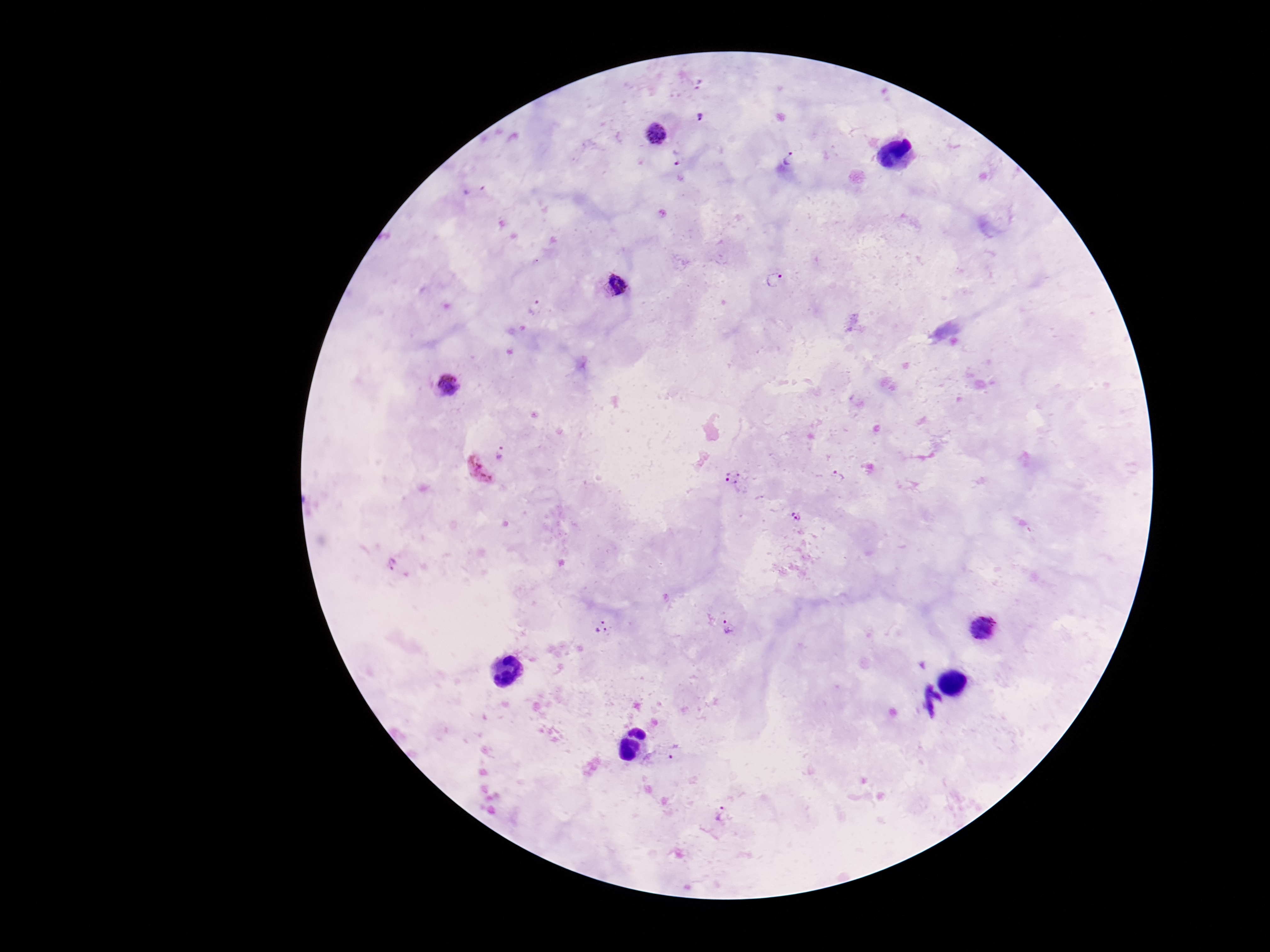

Approximate object centers, in pixels from the top-left corner. Plasmodium parasite locations: (x=697, y=83), (x=699, y=116), (x=656, y=133), (x=679, y=158), (x=788, y=159), (x=473, y=190), (x=774, y=280), (x=616, y=286), (x=535, y=308), (x=449, y=386), (x=502, y=453), (x=477, y=470), (x=836, y=475), (x=734, y=478), (x=797, y=516), (x=394, y=565), (x=601, y=627), (x=730, y=627), (x=983, y=627), (x=674, y=751), (x=720, y=814). Smartphone photograph taken through the microscope eyepiece. Giemsa stain. One field from this slide. Thick peripheral-blood smear. 100x magnification. Image is 1270×952 pixels. Patient malaria status: positive.